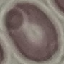

Result: no malaria parasites detected. Thin smear of blood. Giemsa-stained preparation. Cell patch, automatically extracted from a larger field of view and resized to 64 × 64 pixels. Photographed with a smartphone camera at the microscope eyepiece.